Name the parasite shown.
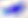

This is Toxoplasma gondii.

Summary:
  - Magnification: 400x
  - Modality: micrograph